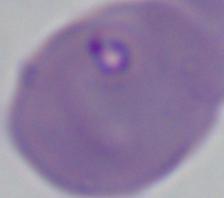

Summary:
  - Modality: micrograph
  - Magnification: 1000x
  - Identification: Babesia